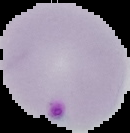

{
  "preparation": "thin blood smear",
  "image_size": "130×133 pixels",
  "malaria_status": "parasitized",
  "image_type": "cell region segmented out of the field of view; surrounding area masked to black"
}